Describe the morphology of the red blood cells.
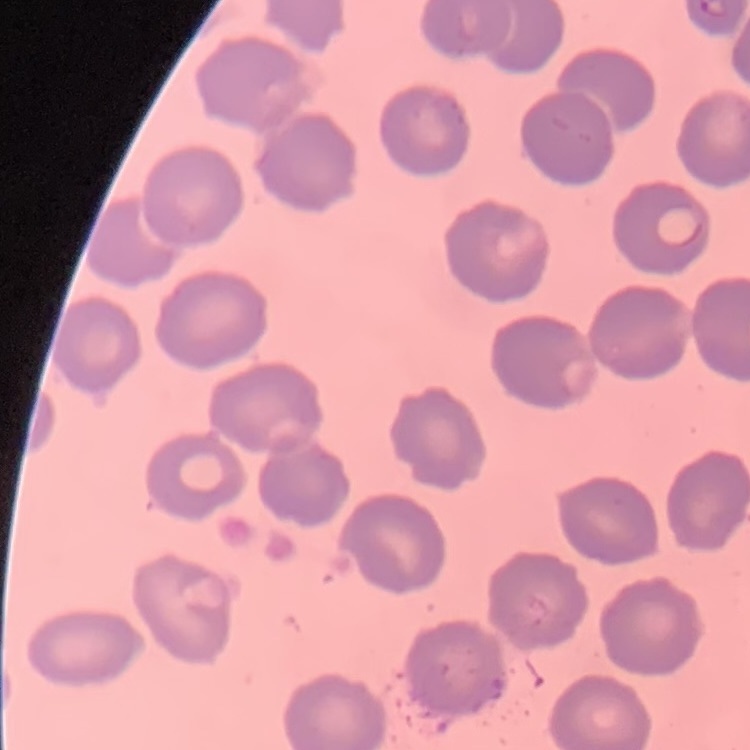
No rouleaux formation.

Summary:
  - Stain: Field's or Giemsa
  - Image type: square crop of a larger photomicrograph
  - Preparation: thin peripheral smear